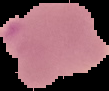

{
  "image_type": "segmented cell region with the area outside set to black",
  "image_size": "109×91 pixels",
  "result": "no Plasmodium parasites detected",
  "preparation": "thin blood smear"
}